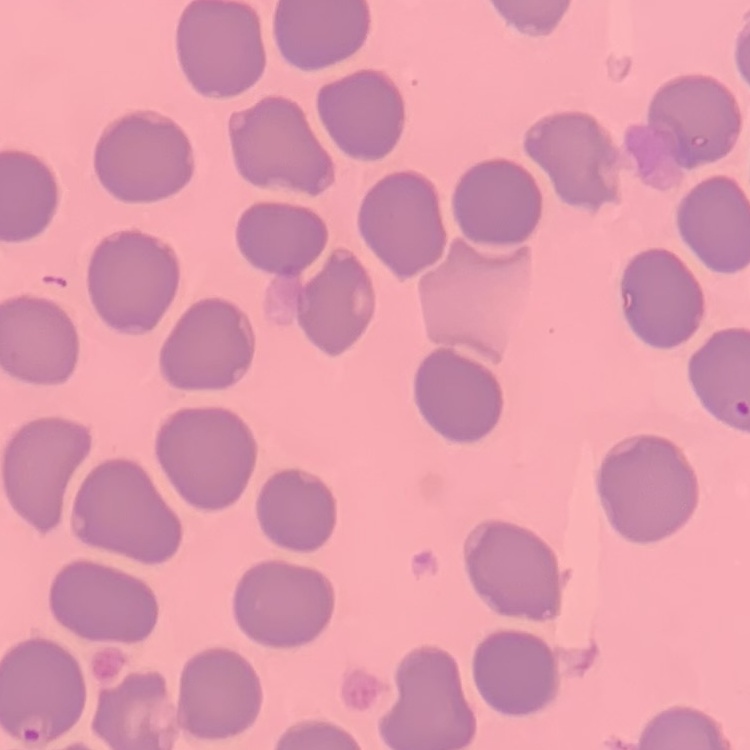

Summary:
  - Erythrocyte morphology: no rouleaux formation
  - Preparation: thin peripheral smear
  - Image type: one tile cut from a larger photomicrograph
  - Stain: Field's or Giemsa